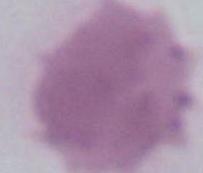

magnification = 1000x
modality = micrograph
identification = red blood cell